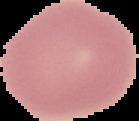
image size = 139×121 pixels
malaria status = uninfected
image type = segmented cell region with the area outside set to black
preparation = thin blood smear